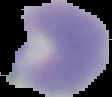
image size = 112×97 pixels
result = no malaria parasites seen
preparation = thin blood film
image type = segmented cell region with the area outside set to black